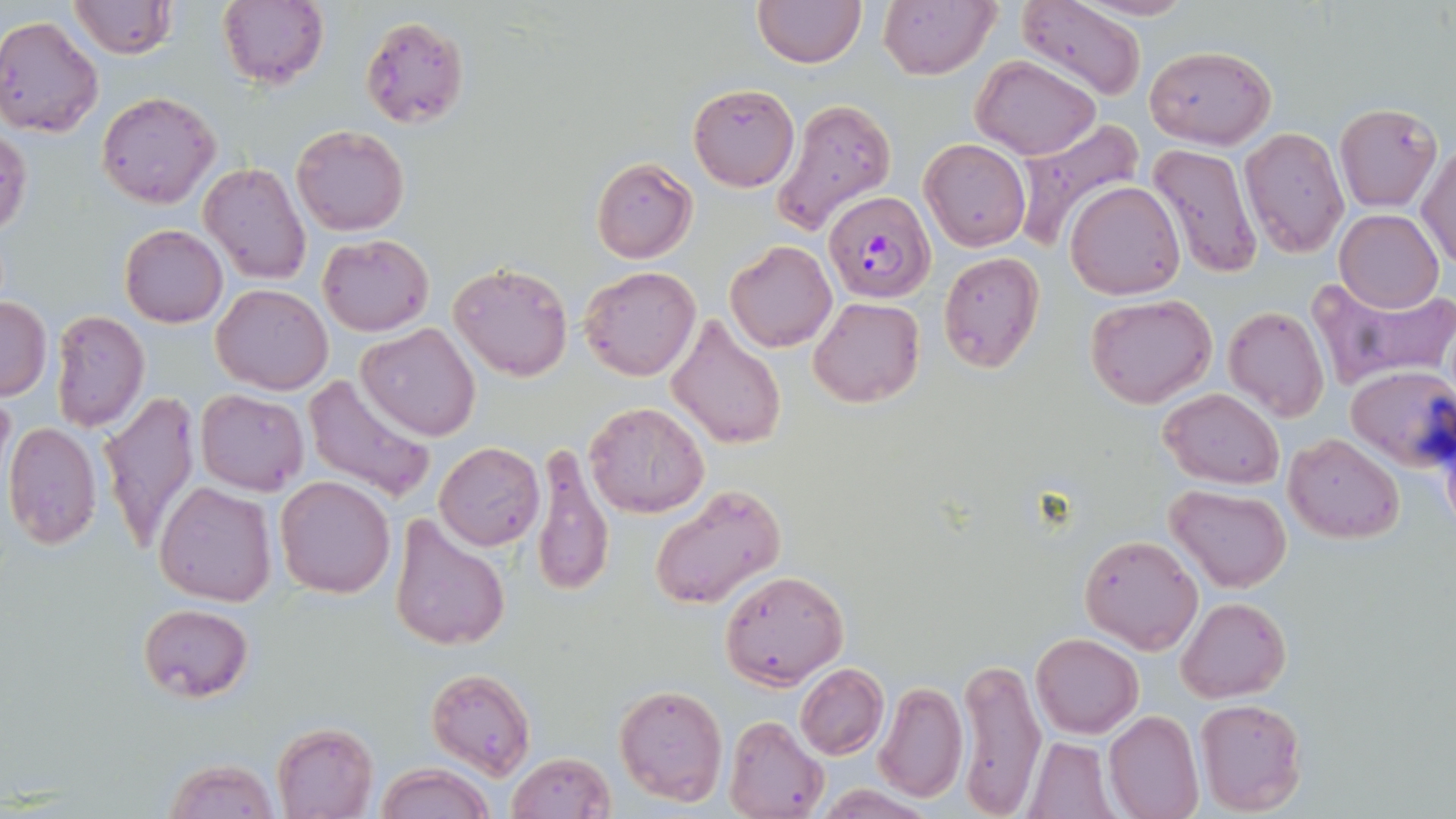
Summary:
  - Coordinate format: approximate bounding boxes as named x1/y1/x2/y2 corners in pixels
  - Plasmodium falciparum-infected red blood cell locations: (x1=824, y1=192, x2=935, y2=303)
  - Uninfected red blood cell locations: (x1=68, y1=0, x2=175, y2=60), (x1=1015, y1=0, x2=1148, y2=103), (x1=215, y1=1, x2=329, y2=90), (x1=752, y1=1, x2=867, y2=68), (x1=877, y1=1, x2=1000, y2=80), (x1=358, y1=14, x2=470, y2=130), (x1=0, y1=17, x2=103, y2=137), (x1=1143, y1=44, x2=1276, y2=147), (x1=972, y1=56, x2=1101, y2=159), (x1=688, y1=84, x2=800, y2=191), (x1=97, y1=92, x2=219, y2=208), (x1=771, y1=97, x2=898, y2=235), (x1=1334, y1=103, x2=1441, y2=210), (x1=1008, y1=119, x2=1143, y2=253), (x1=291, y1=124, x2=410, y2=236), (x1=0, y1=126, x2=32, y2=239), (x1=1239, y1=127, x2=1348, y2=257), (x1=253, y1=128, x2=369, y2=257), (x1=920, y1=139, x2=1030, y2=251), (x1=1418, y1=139, x2=1456, y2=270), (x1=1147, y1=145, x2=1263, y2=280), (x1=589, y1=156, x2=698, y2=264), (x1=199, y1=161, x2=312, y2=286), (x1=1064, y1=181, x2=1184, y2=301), (x1=1334, y1=209, x2=1443, y2=313), (x1=119, y1=224, x2=228, y2=328), (x1=317, y1=234, x2=433, y2=337), (x1=724, y1=241, x2=836, y2=352), (x1=938, y1=251, x2=1044, y2=372), (x1=449, y1=262, x2=573, y2=381), (x1=580, y1=265, x2=701, y2=382), (x1=1306, y1=274, x2=1456, y2=388), (x1=213, y1=283, x2=332, y2=394), (x1=1084, y1=292, x2=1218, y2=409), (x1=0, y1=296, x2=51, y2=399), (x1=809, y1=296, x2=925, y2=407), (x1=1223, y1=305, x2=1329, y2=423), (x1=50, y1=310, x2=148, y2=431), (x1=664, y1=313, x2=786, y2=450), (x1=357, y1=322, x2=481, y2=441), (x1=1345, y1=365, x2=1456, y2=473), (x1=304, y1=371, x2=440, y2=503), (x1=1159, y1=387, x2=1285, y2=489), (x1=195, y1=388, x2=308, y2=495), (x1=99, y1=389, x2=201, y2=551), (x1=584, y1=401, x2=711, y2=517), (x1=3, y1=420, x2=102, y2=548), (x1=1284, y1=432, x2=1402, y2=543), (x1=434, y1=441, x2=545, y2=550), (x1=530, y1=442, x2=614, y2=599), (x1=275, y1=476, x2=395, y2=597), (x1=154, y1=480, x2=277, y2=606), (x1=649, y1=482, x2=787, y2=610), (x1=1166, y1=484, x2=1292, y2=592), (x1=388, y1=513, x2=510, y2=651), (x1=1078, y1=533, x2=1204, y2=654), (x1=720, y1=570, x2=849, y2=689), (x1=1176, y1=597, x2=1290, y2=702), (x1=137, y1=602, x2=253, y2=703), (x1=1030, y1=633, x2=1144, y2=738), (x1=956, y1=655, x2=1045, y2=815), (x1=795, y1=664, x2=888, y2=759), (x1=425, y1=667, x2=536, y2=778), (x1=612, y1=683, x2=728, y2=807), (x1=874, y1=683, x2=967, y2=802), (x1=1193, y1=696, x2=1307, y2=815), (x1=1103, y1=709, x2=1204, y2=819), (x1=725, y1=715, x2=828, y2=819), (x1=270, y1=722, x2=378, y2=819), (x1=1024, y1=738, x2=1116, y2=818), (x1=504, y1=751, x2=615, y2=819), (x1=164, y1=758, x2=280, y2=819), (x1=376, y1=764, x2=494, y2=819)
  - Slide-level diagnosis: Plasmodium falciparum
  - Magnification: 1000x
  - Field of view: one of a larger specimen
  - Preparation: thin blood smear
  - Stain: May-Grünwald-Giemsa
  - Modality: light microscopy
  - Image size: 1456×819 pixels